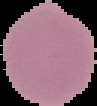

Summary:
  - Result: negative for malaria parasites
  - Image size: 97×106 pixels
  - Preparation: thin blood smear
  - Image type: segmented cell region on a black background